Classify this cell by malaria status.
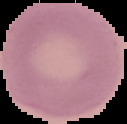

It is uninfected.

preparation: thin blood film
image_size: 127×124 pixels
image_type: segmented cell region with the area outside set to black